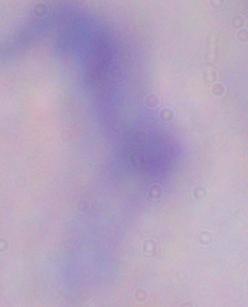

magnification: 1000x
modality: micrograph
identification: trypanosome